Classify this cell by malaria status.
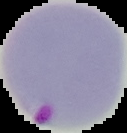
It is parasitized.

Image is 127×133 pixels. From a thin blood smear. Cell region segmented out of the field of view; the surrounding area is masked to black.